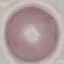
Result: negative for malaria parasites. Acquired by smartphone through the microscope eyepiece. Automatically extracted cell patch, resized to 64 × 64 pixels. Thin smear of blood. Giemsa-stained preparation.